Point out each malaria parasite.
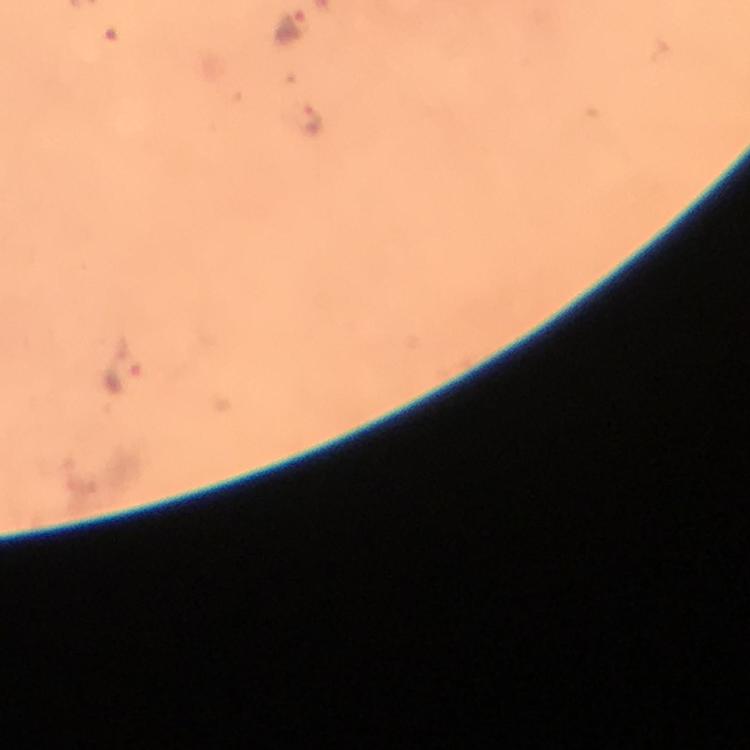
Approximate object centers, in pixels from the top-left corner.
Malaria parasites: (x=293, y=25), (x=309, y=117), (x=124, y=373).

{
  "image_size": "750×750 pixels",
  "magnification": "100x",
  "stain": "Giemsa",
  "preparation": "thick blood film",
  "context": "from a malaria diagnostic workup",
  "capture": "smartphone mounted on the microscope",
  "cropped_from": "a single field of view",
  "immersion_oil": "applied"
}